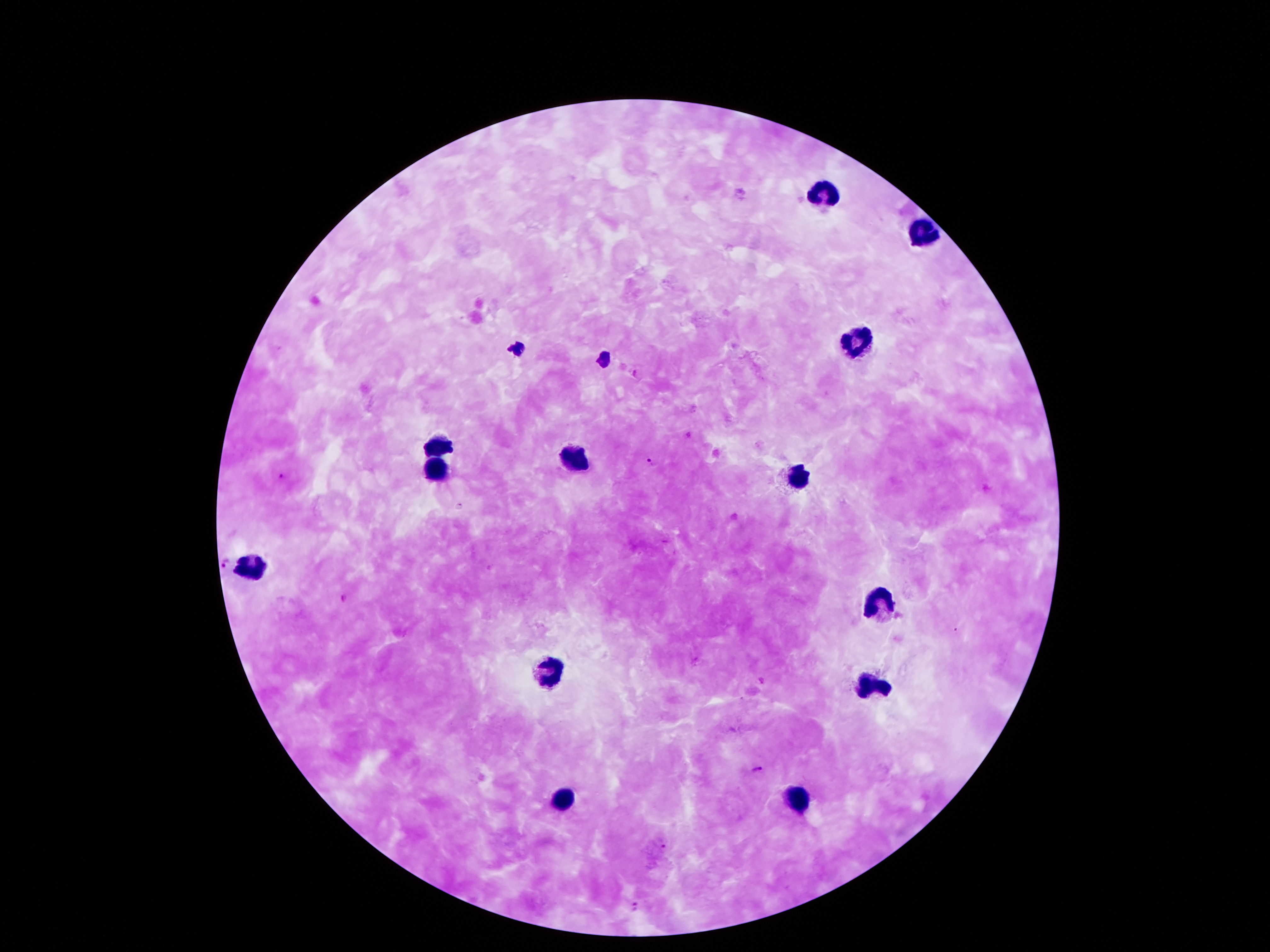
Approximate object centers, in pixels from the top-left corner.
Summary:
  - Malaria parasite locations: (x=635, y=374), (x=651, y=462), (x=283, y=475), (x=225, y=564), (x=344, y=597), (x=757, y=769), (x=663, y=847), (x=635, y=906)
  - Leukocyte locations: (x=821, y=196), (x=924, y=232), (x=858, y=340), (x=438, y=446), (x=576, y=452), (x=435, y=468), (x=799, y=480), (x=251, y=570), (x=880, y=600), (x=549, y=668), (x=874, y=684), (x=796, y=797), (x=562, y=799)
  - Capture: smartphone camera through the microscope eyepiece
  - Stain: Giemsa
  - Magnification: 100x
  - Image size: 1270×952 pixels
  - Field of view: single
  - Preparation: thick peripheral-blood smear
  - Patient malaria status: positive for Plasmodium falciparum